Report the malaria status of this cell.
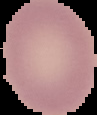

It is uninfected.

image_size: 97×115 pixels
preparation: thin blood film
image_type: cell region segmented out of the field of view; surrounding area masked to black